Locate every Plasmodium parasite.
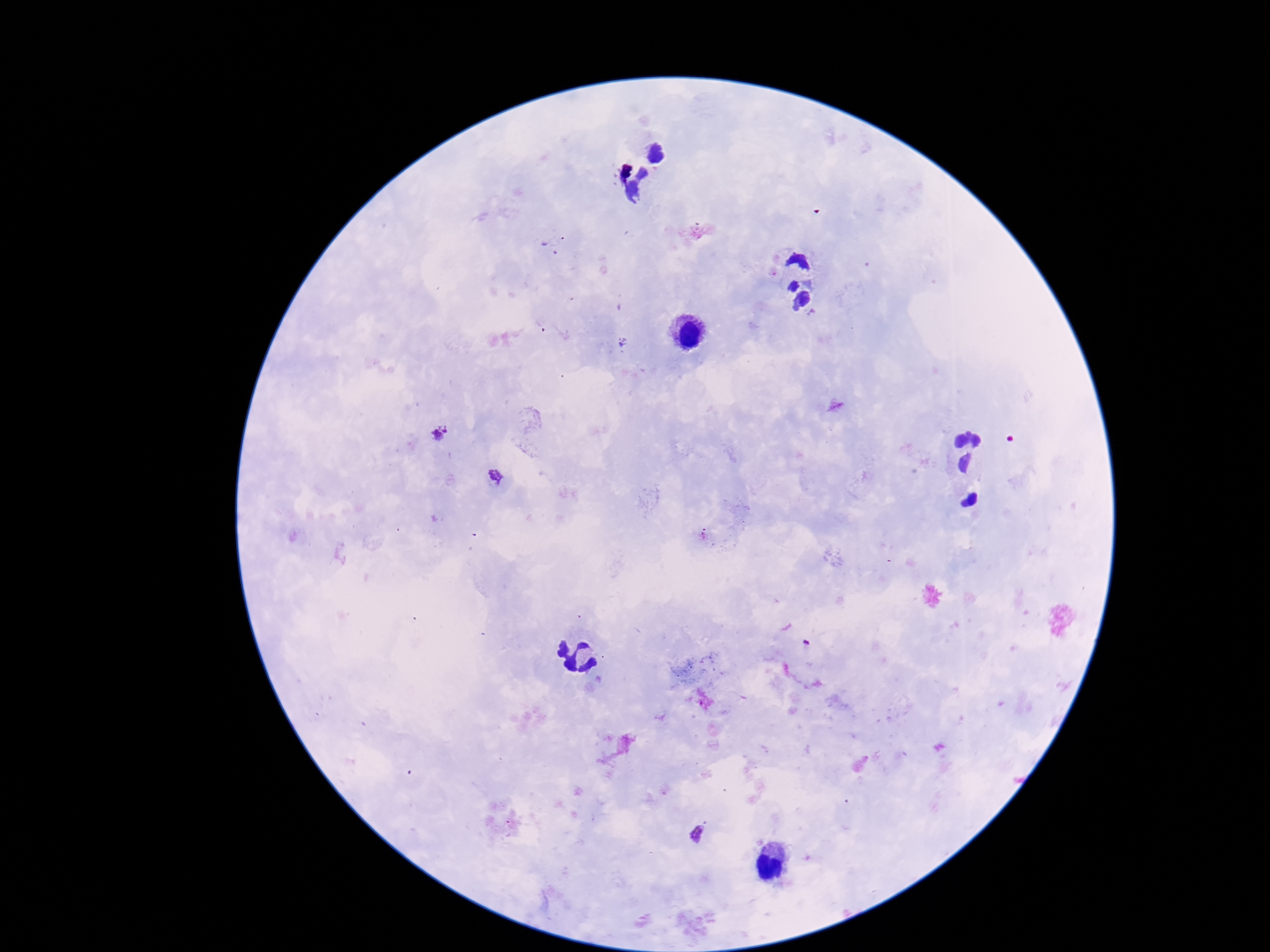

Approximate centers as (x, y) in pixels.
Plasmodium parasites: (438, 433), (495, 477), (697, 833).

magnification: 100x
preparation: thick blood smear
patient_malaria_status: infected
field_of_view: one from this slide
capture: smartphone camera through the microscope eyepiece
image_size: 1270×952 pixels
stain: Giemsa